Identify the parasite.
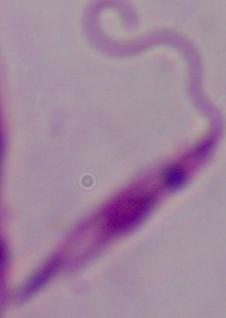
Leishmania.

magnification = 1000x
modality = photomicrograph